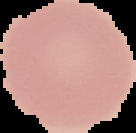

Cell region segmented out of the field of view; the surrounding area is masked to black. From a thin blood smear. Result: negative for malaria parasites. Image is 136×133 pixels.